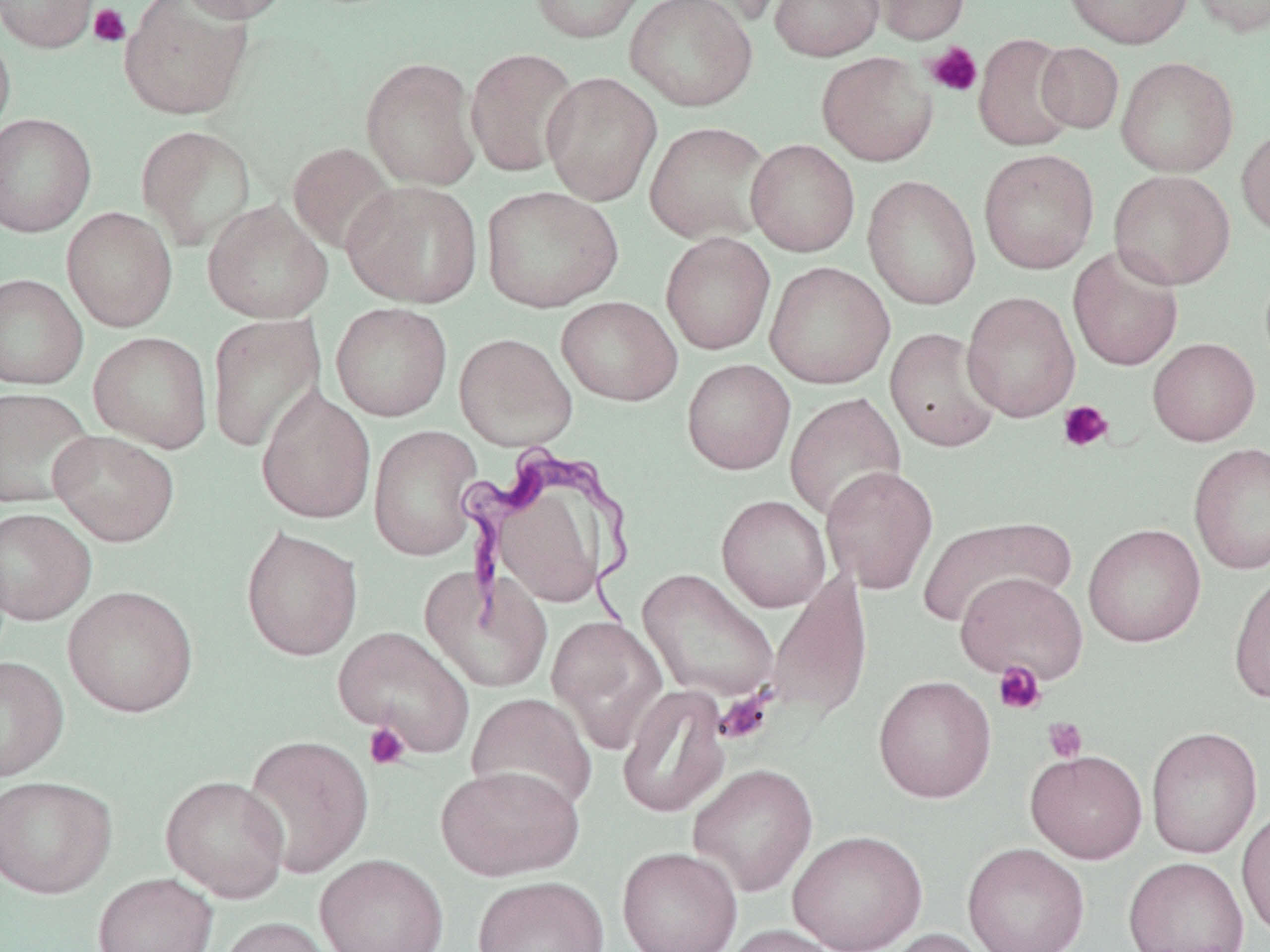
{
  "trypanosoma_brucei_locations": "approximate bounding boxes as named x1/y1/x2/y2 corners in pixels: (x1=459, y1=447, x2=640, y2=631)",
  "slide_level_diagnosis": "Trypanosoma brucei",
  "field_of_view": "single",
  "magnification": "1000x",
  "stain": "May-Grünwald-Giemsa",
  "image_size": "1270×952 pixels",
  "uninfected_red_blood_cell_locations": "approximate bounding boxes as named x1/y1/x2/y2 corners in pixels: (x1=0, y1=0, x2=100, y2=52), (x1=120, y1=0, x2=253, y2=120), (x1=175, y1=0, x2=292, y2=23), (x1=528, y1=0, x2=649, y2=44), (x1=624, y1=0, x2=758, y2=112), (x1=666, y1=0, x2=787, y2=29), (x1=769, y1=0, x2=884, y2=61), (x1=864, y1=0, x2=971, y2=45), (x1=1062, y1=0, x2=1193, y2=48), (x1=1186, y1=0, x2=1270, y2=37), (x1=0, y1=24, x2=16, y2=143), (x1=973, y1=33, x2=1078, y2=152), (x1=1035, y1=42, x2=1124, y2=134), (x1=465, y1=47, x2=581, y2=177), (x1=817, y1=51, x2=938, y2=166), (x1=360, y1=56, x2=482, y2=190), (x1=1116, y1=56, x2=1239, y2=177), (x1=541, y1=70, x2=662, y2=206), (x1=0, y1=113, x2=97, y2=238), (x1=644, y1=121, x2=772, y2=244), (x1=135, y1=124, x2=257, y2=250), (x1=1237, y1=125, x2=1270, y2=239), (x1=745, y1=139, x2=860, y2=256), (x1=287, y1=142, x2=398, y2=255), (x1=978, y1=148, x2=1100, y2=274), (x1=1109, y1=170, x2=1236, y2=289), (x1=863, y1=175, x2=981, y2=310), (x1=341, y1=179, x2=483, y2=308), (x1=481, y1=185, x2=623, y2=313), (x1=202, y1=199, x2=333, y2=324), (x1=62, y1=207, x2=177, y2=332), (x1=660, y1=231, x2=776, y2=355), (x1=1068, y1=245, x2=1184, y2=371), (x1=764, y1=262, x2=895, y2=389), (x1=0, y1=273, x2=88, y2=390), (x1=961, y1=291, x2=1081, y2=421), (x1=556, y1=295, x2=682, y2=406), (x1=330, y1=302, x2=452, y2=422), (x1=206, y1=312, x2=325, y2=454), (x1=885, y1=328, x2=1002, y2=452), (x1=89, y1=331, x2=213, y2=452), (x1=454, y1=332, x2=577, y2=451), (x1=1148, y1=338, x2=1260, y2=446), (x1=682, y1=359, x2=795, y2=474), (x1=256, y1=386, x2=376, y2=524), (x1=0, y1=387, x2=95, y2=509), (x1=784, y1=392, x2=906, y2=523), (x1=368, y1=424, x2=483, y2=561), (x1=48, y1=430, x2=180, y2=547), (x1=1188, y1=441, x2=1270, y2=576), (x1=820, y1=465, x2=939, y2=594), (x1=495, y1=493, x2=603, y2=610), (x1=716, y1=495, x2=831, y2=612), (x1=0, y1=507, x2=96, y2=625), (x1=916, y1=517, x2=1075, y2=629), (x1=1083, y1=523, x2=1206, y2=648), (x1=240, y1=525, x2=363, y2=662), (x1=419, y1=567, x2=553, y2=693), (x1=1228, y1=567, x2=1270, y2=704), (x1=637, y1=568, x2=779, y2=704), (x1=955, y1=571, x2=1088, y2=683), (x1=765, y1=572, x2=874, y2=722), (x1=62, y1=585, x2=199, y2=718), (x1=547, y1=616, x2=667, y2=753), (x1=333, y1=625, x2=474, y2=756), (x1=0, y1=655, x2=69, y2=782), (x1=873, y1=675, x2=996, y2=803), (x1=617, y1=684, x2=731, y2=819), (x1=466, y1=693, x2=598, y2=815), (x1=1146, y1=726, x2=1262, y2=858), (x1=240, y1=733, x2=374, y2=879), (x1=1025, y1=749, x2=1147, y2=863), (x1=686, y1=763, x2=818, y2=897), (x1=435, y1=765, x2=585, y2=881), (x1=0, y1=775, x2=116, y2=898), (x1=160, y1=775, x2=290, y2=902), (x1=1236, y1=806, x2=1270, y2=941), (x1=787, y1=829, x2=927, y2=952), (x1=962, y1=842, x2=1091, y2=952), (x1=617, y1=846, x2=742, y2=952), (x1=314, y1=854, x2=448, y2=952), (x1=1123, y1=856, x2=1249, y2=952), (x1=93, y1=872, x2=218, y2=952), (x1=472, y1=875, x2=609, y2=952), (x1=216, y1=916, x2=341, y2=952), (x1=718, y1=924, x2=845, y2=952), (x1=880, y1=928, x2=995, y2=952)",
  "modality": "optical microscopy",
  "platelet_locations": "approximate bounding boxes as named x1/y1/x2/y2 corners in pixels: (x1=89, y1=3, x2=131, y2=47), (x1=924, y1=42, x2=983, y2=97), (x1=1057, y1=400, x2=1114, y2=453), (x1=992, y1=662, x2=1046, y2=716), (x1=715, y1=689, x2=775, y2=745), (x1=1042, y1=717, x2=1087, y2=763), (x1=364, y1=722, x2=411, y2=770)",
  "preparation": "thin blood film"
}